Name the blood parasite species.
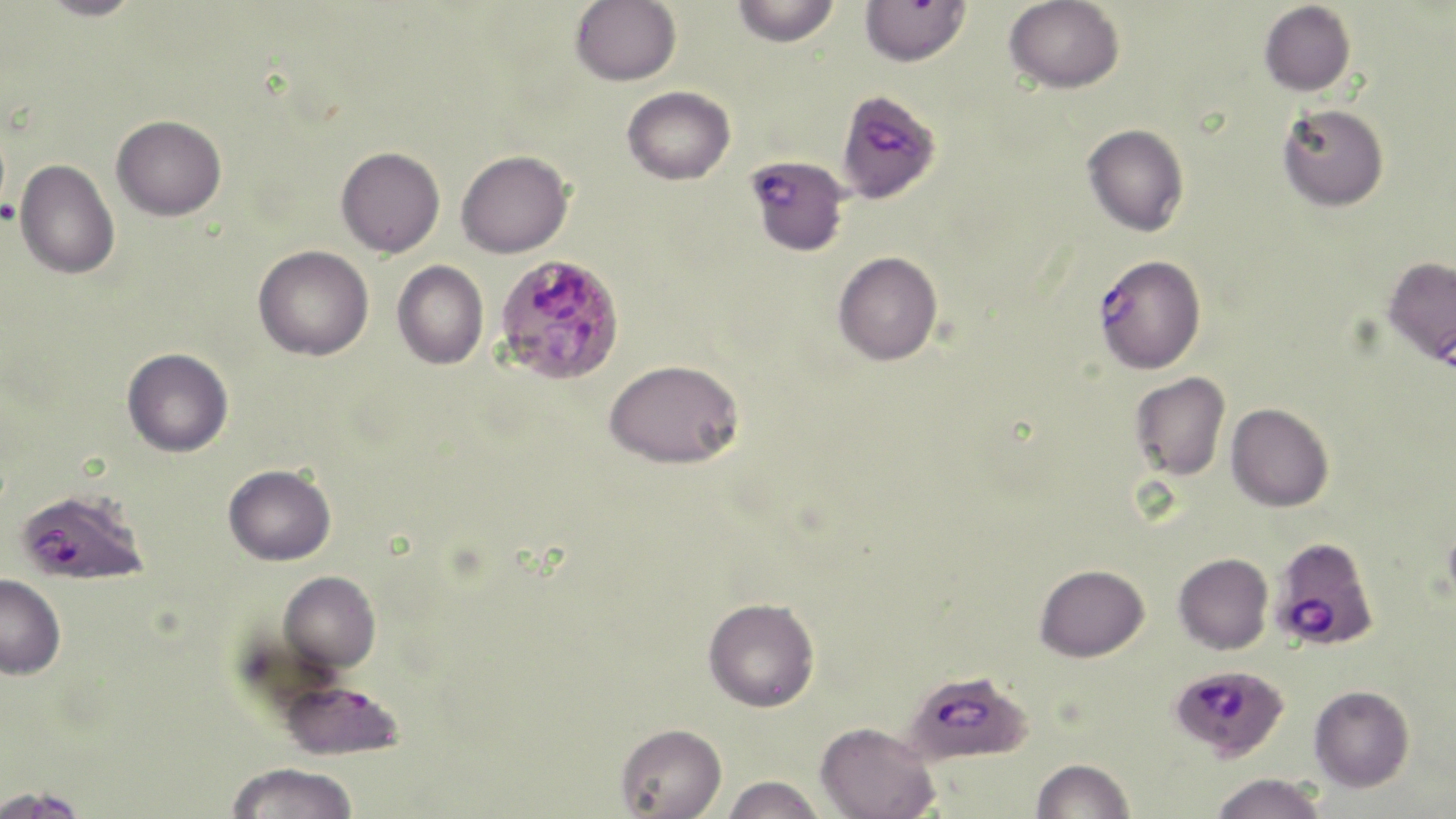

Plasmodium falciparum.

Approximate bounding boxes as named x1/y1/x2/y2 corners in pixels. Platelet locations: (x1=0, y1=200, x2=19, y2=225). Plasmodium falciparum-infected red blood cell locations: (x1=847, y1=96, x2=933, y2=206), (x1=748, y1=152, x2=858, y2=247), (x1=1093, y1=253, x2=1206, y2=374), (x1=494, y1=254, x2=626, y2=386), (x1=15, y1=489, x2=148, y2=586), (x1=1270, y1=536, x2=1379, y2=651), (x1=1170, y1=664, x2=1290, y2=761), (x1=901, y1=670, x2=1033, y2=765), (x1=278, y1=679, x2=405, y2=761). Uninfected red blood cell locations: (x1=37, y1=0, x2=146, y2=21), (x1=570, y1=0, x2=681, y2=86), (x1=731, y1=0, x2=840, y2=47), (x1=1004, y1=0, x2=1125, y2=93), (x1=860, y1=1, x2=971, y2=66), (x1=1259, y1=1, x2=1356, y2=96), (x1=622, y1=86, x2=735, y2=185), (x1=1277, y1=103, x2=1389, y2=211), (x1=112, y1=115, x2=226, y2=220), (x1=1083, y1=124, x2=1189, y2=237), (x1=335, y1=146, x2=445, y2=257), (x1=456, y1=149, x2=573, y2=258), (x1=15, y1=159, x2=120, y2=279), (x1=253, y1=244, x2=373, y2=360), (x1=833, y1=251, x2=942, y2=365), (x1=1382, y1=256, x2=1456, y2=366), (x1=392, y1=260, x2=488, y2=369), (x1=122, y1=348, x2=233, y2=456), (x1=604, y1=358, x2=744, y2=469), (x1=1130, y1=372, x2=1230, y2=481), (x1=1225, y1=403, x2=1334, y2=512), (x1=223, y1=464, x2=336, y2=566), (x1=1174, y1=553, x2=1274, y2=654), (x1=1035, y1=563, x2=1149, y2=662), (x1=279, y1=571, x2=380, y2=672), (x1=0, y1=574, x2=66, y2=679), (x1=702, y1=597, x2=820, y2=712), (x1=1309, y1=685, x2=1414, y2=792), (x1=816, y1=721, x2=940, y2=818), (x1=615, y1=722, x2=727, y2=819), (x1=1031, y1=758, x2=1135, y2=818), (x1=226, y1=762, x2=358, y2=819), (x1=1210, y1=772, x2=1330, y2=819), (x1=720, y1=775, x2=827, y2=819), (x1=0, y1=785, x2=90, y2=819). One field of a larger specimen. 1000x magnification. May-Grünwald-Giemsa-stained preparation. Optical microscopy. Image is 1456×819 pixels. Thin blood film.